Outline each Plasmodium vivax-infected red blood cell.
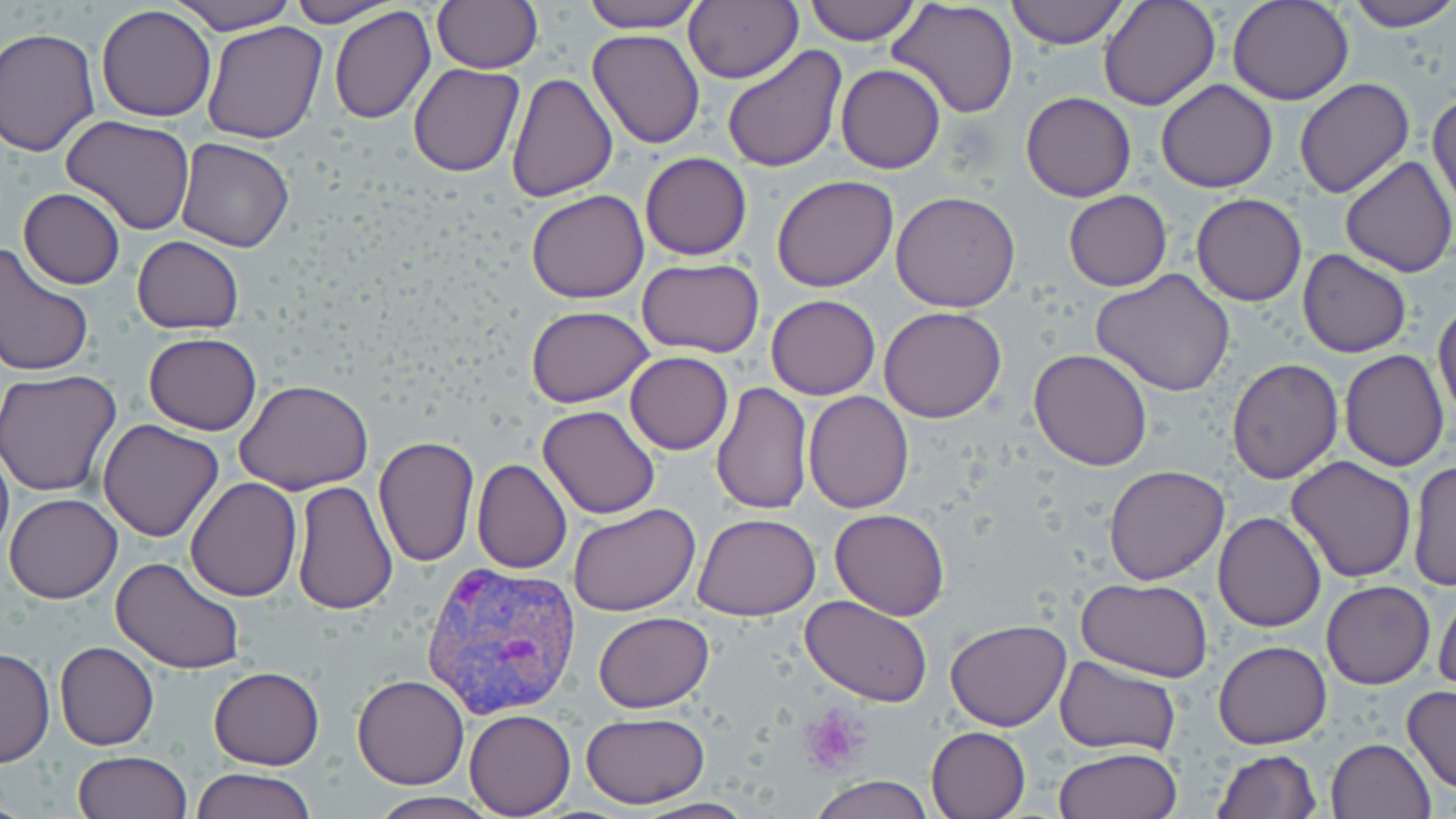
Approximate bounding boxes as (x1,y1)-(x2,y2) corner pairs in pixels.
Plasmodium vivax-infected red blood cells: (419,557)-(581,720).

Platelet locations: (799,707)-(866,777). Uninfected red blood cell locations: (171,0)-(293,35), (283,0)-(400,26), (583,0)-(706,33), (683,0)-(800,85), (801,0)-(920,44), (1003,0)-(1128,49), (1097,0)-(1220,110), (1228,0)-(1353,104), (1342,0)-(1456,32), (889,1)-(1020,118), (432,2)-(542,73), (95,5)-(216,121), (328,5)-(437,125), (202,21)-(329,144), (0,26)-(100,157), (588,30)-(706,148), (722,46)-(847,172), (408,63)-(524,178), (836,64)-(946,173), (505,72)-(619,203), (1294,78)-(1414,199), (1156,79)-(1278,194), (1020,92)-(1137,202), (1428,92)-(1456,211), (62,114)-(196,235), (174,138)-(296,253), (640,152)-(751,259), (1339,155)-(1455,278), (771,175)-(899,293), (19,188)-(125,290), (527,189)-(648,304), (890,191)-(1021,312), (1062,191)-(1172,292), (1191,194)-(1307,306), (131,236)-(244,334), (0,242)-(95,379), (1299,249)-(1411,358), (637,257)-(764,358), (1092,268)-(1238,395), (766,295)-(881,400), (1433,299)-(1456,421), (526,306)-(654,407), (878,307)-(1006,424), (143,333)-(263,435), (1029,349)-(1153,470), (1339,350)-(1449,472), (625,352)-(733,455), (1227,359)-(1342,483), (0,370)-(123,496), (235,382)-(372,495), (711,382)-(811,516), (803,390)-(915,512), (538,403)-(661,520), (97,418)-(224,541), (0,435)-(13,562), (373,436)-(480,569), (1285,455)-(1417,583), (472,458)-(570,573), (1408,460)-(1454,595), (1103,465)-(1231,585), (186,478)-(302,602), (291,480)-(397,614), (1155,480)-(1325,609), (5,493)-(122,604), (569,503)-(700,617), (829,508)-(949,619), (1213,510)-(1327,631), (694,513)-(821,620), (111,556)-(246,675), (1078,577)-(1212,682), (1321,578)-(1436,689), (1432,585)-(1456,694), (800,595)-(933,709), (592,611)-(714,712), (945,619)-(1072,731), (54,642)-(159,750), (1212,642)-(1331,749), (0,646)-(54,768), (1054,656)-(1182,755), (208,666)-(324,769), (350,675)-(470,789), (1402,685)-(1456,798), (464,708)-(575,817), (581,714)-(710,808), (927,726)-(1031,819), (1325,738)-(1436,819), (1054,746)-(1182,819), (1212,748)-(1322,818), (72,751)-(192,818), (190,767)-(316,819), (809,775)-(933,818), (365,793)-(503,819), (635,798)-(756,817). Slide-level diagnosis: Plasmodium vivax. Image is 1456×819 pixels. 1000x magnification. Thin blood smear. Optical microscopy. May-Grünwald-Giemsa-stained preparation. One field of a larger specimen.